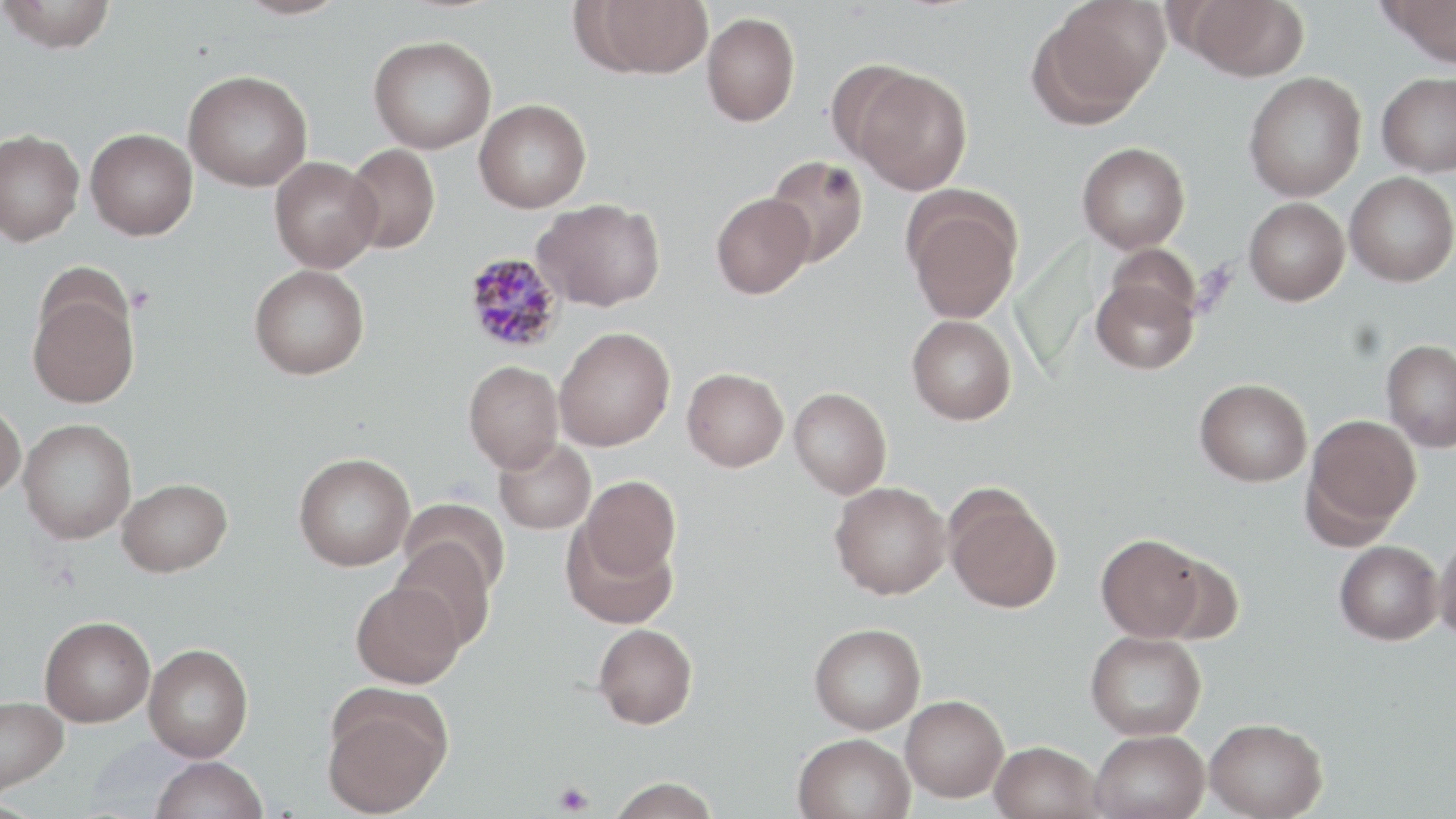 Approximate bounding boxes as named x1/y1/x2/y2 corners in pixels. Platelet locations: (x1=554, y1=780, x2=594, y2=815). Uninfected red blood cell locations: (x1=0, y1=0, x2=118, y2=53), (x1=235, y1=0, x2=350, y2=20), (x1=584, y1=0, x2=715, y2=78), (x1=1182, y1=0, x2=1309, y2=80), (x1=1376, y1=0, x2=1456, y2=66), (x1=1032, y1=2, x2=1167, y2=124), (x1=702, y1=11, x2=800, y2=126), (x1=368, y1=35, x2=496, y2=153), (x1=825, y1=59, x2=927, y2=171), (x1=850, y1=67, x2=973, y2=194), (x1=183, y1=70, x2=313, y2=191), (x1=1243, y1=72, x2=1366, y2=202), (x1=1377, y1=72, x2=1456, y2=176), (x1=474, y1=99, x2=591, y2=212), (x1=85, y1=127, x2=198, y2=239), (x1=0, y1=129, x2=84, y2=246), (x1=1077, y1=141, x2=1190, y2=254), (x1=343, y1=143, x2=440, y2=253), (x1=765, y1=155, x2=868, y2=267), (x1=270, y1=156, x2=383, y2=273), (x1=1345, y1=171, x2=1456, y2=287), (x1=711, y1=192, x2=815, y2=298), (x1=902, y1=192, x2=1023, y2=323), (x1=1244, y1=197, x2=1350, y2=305), (x1=533, y1=198, x2=665, y2=311), (x1=1105, y1=243, x2=1202, y2=330), (x1=249, y1=264, x2=370, y2=379), (x1=1091, y1=276, x2=1198, y2=375), (x1=27, y1=286, x2=140, y2=408), (x1=907, y1=315, x2=1016, y2=424), (x1=554, y1=327, x2=675, y2=450), (x1=1382, y1=339, x2=1456, y2=451), (x1=463, y1=360, x2=564, y2=473), (x1=681, y1=367, x2=788, y2=472), (x1=1195, y1=378, x2=1312, y2=486), (x1=789, y1=387, x2=892, y2=499), (x1=0, y1=399, x2=26, y2=498), (x1=1304, y1=413, x2=1421, y2=537), (x1=18, y1=418, x2=137, y2=544), (x1=493, y1=437, x2=597, y2=534), (x1=294, y1=452, x2=415, y2=571), (x1=579, y1=475, x2=681, y2=578), (x1=117, y1=478, x2=232, y2=577), (x1=830, y1=481, x2=951, y2=599), (x1=944, y1=487, x2=1062, y2=614), (x1=398, y1=498, x2=510, y2=596), (x1=561, y1=521, x2=678, y2=629), (x1=1434, y1=532, x2=1456, y2=645), (x1=1096, y1=534, x2=1208, y2=642), (x1=391, y1=537, x2=497, y2=649), (x1=1334, y1=540, x2=1443, y2=645), (x1=1152, y1=552, x2=1245, y2=646), (x1=350, y1=580, x2=464, y2=688), (x1=39, y1=617, x2=155, y2=726), (x1=809, y1=622, x2=926, y2=734), (x1=593, y1=623, x2=698, y2=728), (x1=1085, y1=630, x2=1207, y2=740), (x1=143, y1=643, x2=253, y2=761), (x1=321, y1=689, x2=452, y2=818), (x1=901, y1=695, x2=1009, y2=802), (x1=0, y1=696, x2=69, y2=795), (x1=1205, y1=717, x2=1328, y2=818), (x1=1089, y1=729, x2=1210, y2=819), (x1=792, y1=732, x2=916, y2=819), (x1=990, y1=741, x2=1104, y2=819), (x1=150, y1=756, x2=268, y2=819), (x1=606, y1=777, x2=721, y2=819). Plasmodium malariae-infected red blood cell locations: (x1=463, y1=251, x2=565, y2=354). Slide-level diagnosis: Plasmodium malariae. May-Grünwald-Giemsa-stained preparation. Single field of view. Optical microscopy. 1000x magnification. Image is 1456×819 pixels. Thin blood smear.